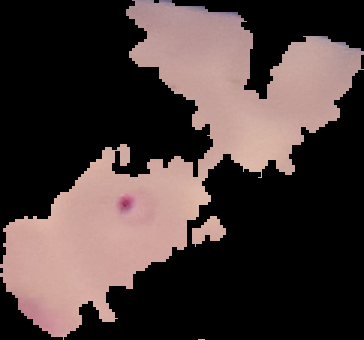 Cell region segmented out of the field of view; the surrounding area is masked to black. Image is 364×340 pixels. Result: malaria parasites detected. From a thin blood film.